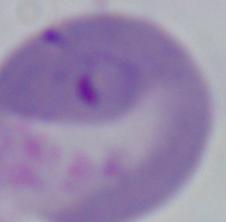 A Babesia parasite is shown. 1000x magnification. Photomicrograph.